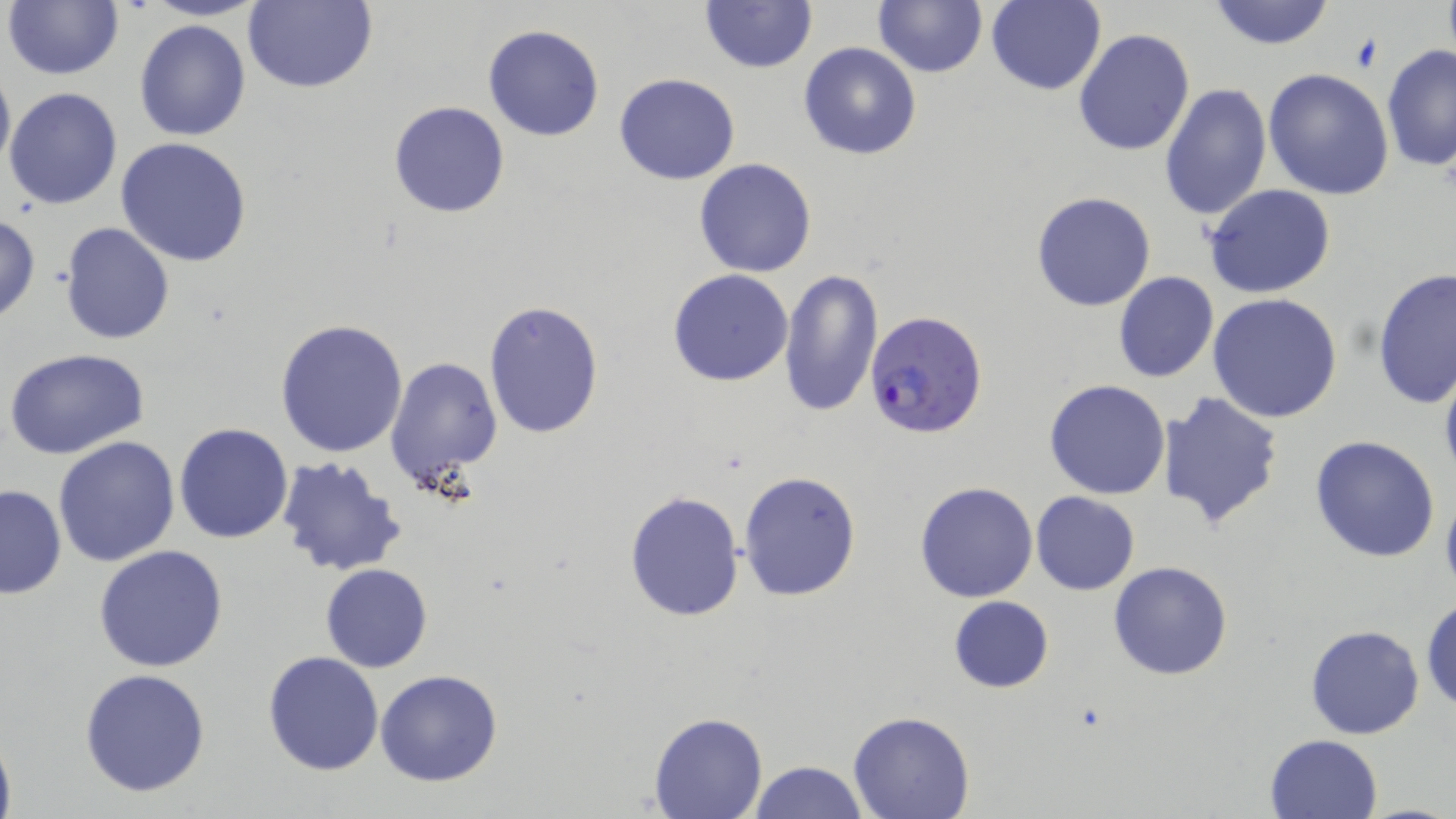

slide-level diagnosis = Plasmodium falciparum
uninfected red blood cell locations = approximate bounding boxes as named x1/y1/x2/y2 corners in pixels: (x1=5, y1=0, x2=124, y2=81), (x1=141, y1=0, x2=268, y2=21), (x1=871, y1=0, x2=988, y2=77), (x1=1207, y1=0, x2=1336, y2=50), (x1=241, y1=1, x2=378, y2=93), (x1=700, y1=1, x2=817, y2=73), (x1=984, y1=1, x2=1107, y2=96), (x1=134, y1=19, x2=252, y2=141), (x1=482, y1=24, x2=604, y2=142), (x1=1073, y1=27, x2=1195, y2=157), (x1=797, y1=41, x2=922, y2=161), (x1=1381, y1=42, x2=1456, y2=175), (x1=0, y1=62, x2=14, y2=179), (x1=1263, y1=68, x2=1394, y2=200), (x1=614, y1=73, x2=741, y2=185), (x1=1159, y1=83, x2=1272, y2=221), (x1=4, y1=86, x2=123, y2=210), (x1=388, y1=100, x2=511, y2=218), (x1=116, y1=138, x2=255, y2=267), (x1=694, y1=158, x2=816, y2=278), (x1=1204, y1=184, x2=1336, y2=299), (x1=1031, y1=191, x2=1157, y2=312), (x1=0, y1=214, x2=42, y2=324), (x1=60, y1=222, x2=175, y2=345), (x1=1373, y1=267, x2=1456, y2=411), (x1=667, y1=269, x2=794, y2=387), (x1=778, y1=270, x2=884, y2=417), (x1=1114, y1=272, x2=1219, y2=383), (x1=1208, y1=294, x2=1344, y2=424), (x1=482, y1=300, x2=604, y2=439), (x1=275, y1=317, x2=407, y2=457), (x1=5, y1=348, x2=150, y2=461), (x1=384, y1=356, x2=504, y2=489), (x1=1438, y1=359, x2=1456, y2=491), (x1=1044, y1=380, x2=1171, y2=500), (x1=1157, y1=391, x2=1283, y2=529), (x1=174, y1=422, x2=293, y2=544), (x1=1310, y1=434, x2=1441, y2=561), (x1=54, y1=437, x2=180, y2=569), (x1=275, y1=453, x2=407, y2=577), (x1=737, y1=470, x2=862, y2=601), (x1=915, y1=481, x2=1039, y2=602), (x1=0, y1=485, x2=67, y2=598), (x1=624, y1=490, x2=745, y2=622), (x1=1031, y1=491, x2=1140, y2=595), (x1=94, y1=545, x2=228, y2=672), (x1=1108, y1=561, x2=1233, y2=680), (x1=321, y1=563, x2=433, y2=673), (x1=948, y1=595, x2=1054, y2=694), (x1=1422, y1=596, x2=1455, y2=713), (x1=1305, y1=624, x2=1425, y2=741), (x1=262, y1=651, x2=384, y2=775), (x1=79, y1=667, x2=212, y2=798), (x1=375, y1=670, x2=504, y2=787), (x1=848, y1=712, x2=975, y2=819), (x1=649, y1=713, x2=766, y2=819), (x1=0, y1=726, x2=16, y2=819), (x1=1264, y1=734, x2=1384, y2=819), (x1=749, y1=760, x2=869, y2=818)
magnification = 1000x
preparation = thin blood film
image size = 1456×819 pixels
Plasmodium falciparum-infected red blood cell locations = approximate bounding boxes as named x1/y1/x2/y2 corners in pixels: (x1=865, y1=310, x2=990, y2=439)
stain = May-Grünwald-Giemsa
field of view = single
modality = light microscopy